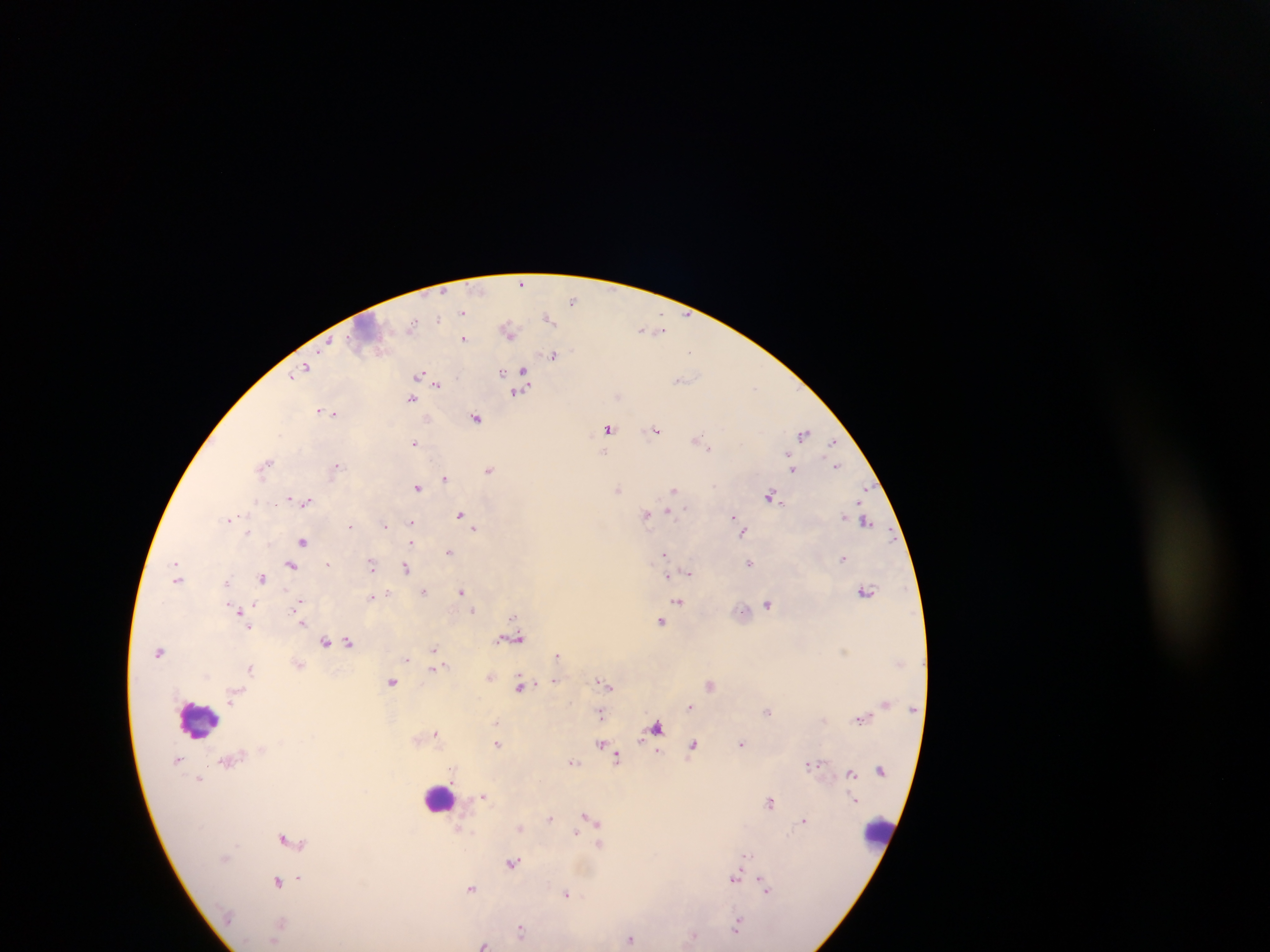

leukocyte locations = approximate centers as (x, y) in pixels: (198, 719), (440, 797), (877, 829)
preparation = thick blood film
capture = mobile-phone photograph through a microscope
country = Ghana
malaria parasite locations = approximate centers as (x, y) in pixels: (522, 283), (572, 300), (462, 312), (548, 317), (438, 318), (411, 325), (508, 330), (642, 330), (661, 330), (463, 338), (690, 350), (553, 355), (306, 367), (523, 370), (503, 372), (418, 374), (292, 376), (680, 380), (437, 383), (755, 387), (516, 393), (411, 398), (319, 410), (335, 413), (476, 417), (609, 428), (655, 429), (803, 433), (696, 440), (414, 443), (703, 443), (832, 443), (708, 447), (834, 451), (605, 453), (266, 464), (836, 465), (334, 466), (792, 469), (490, 470), (445, 478), (714, 485), (417, 488), (618, 489), (673, 489), (863, 492), (770, 495), (290, 499), (308, 501), (256, 502), (685, 507), (669, 511), (460, 514), (646, 514), (229, 518), (733, 518), (410, 521), (865, 521), (351, 525), (385, 526), (474, 527), (739, 527), (247, 531), (742, 532), (303, 542), (411, 543), (449, 551), (664, 554), (843, 559), (175, 563), (749, 563), (291, 565), (327, 565), (372, 566), (406, 568), (689, 572), (667, 576), (263, 578), (177, 579), (227, 582), (866, 591), (386, 592), (424, 592), (461, 592), (371, 597), (299, 602), (677, 602), (768, 604), (240, 611), (473, 611), (302, 622), (661, 622), (248, 627), (514, 638), (326, 641), (349, 642), (434, 650), (159, 651), (843, 651), (557, 655), (407, 659), (436, 667), (250, 670), (489, 677), (554, 681), (601, 681), (392, 683), (607, 684), (710, 684), (521, 685), (690, 706), (767, 711), (600, 714), (861, 719), (496, 722), (656, 726), (435, 732), (742, 742), (497, 744), (602, 744), (693, 745), (658, 751), (617, 758), (573, 762), (810, 764), (851, 773), (199, 779), (483, 795), (855, 799), (770, 802), (587, 817), (550, 818), (805, 820), (576, 832), (284, 838), (599, 844), (746, 856), (513, 862), (299, 877), (734, 877), (277, 882), (763, 882), (766, 888), (472, 889), (567, 893), (738, 926), (522, 931), (692, 936), (631, 939), (483, 944)
image size = 1270×952 pixels
field of view = single